Comment on the morphology of the red blood cells.
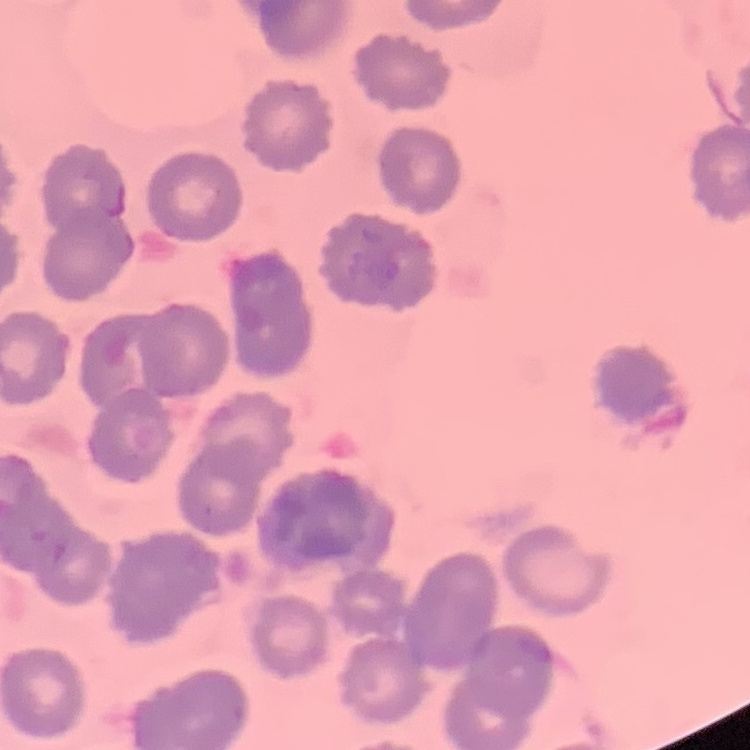

They show no rouleaux formation.

{
  "image_type": "square crop of a larger photomicrograph",
  "stain": "Field's or Giemsa",
  "preparation": "thin peripheral smear"
}